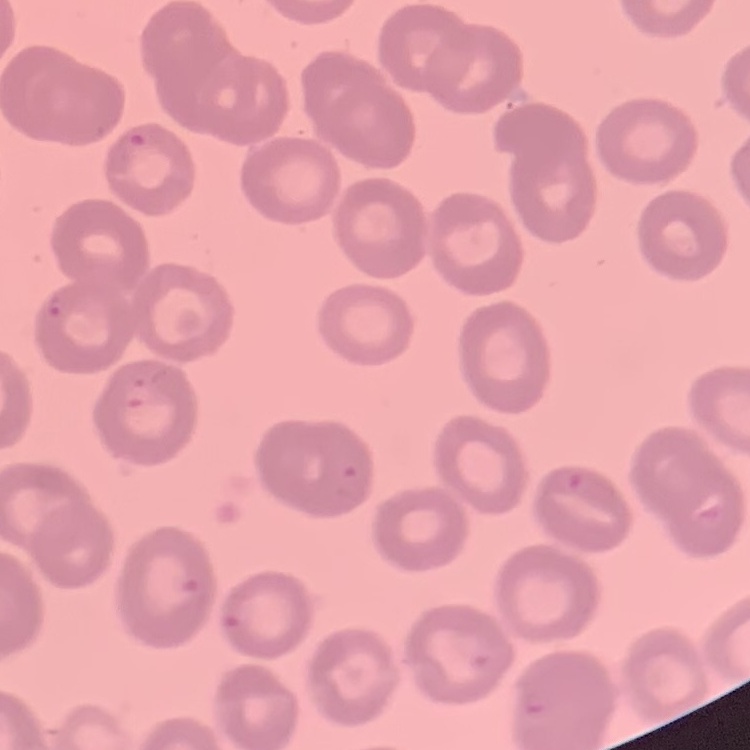
Summary:
  - Erythrocyte morphology: no rouleaux formation
  - Stain: Field's or Giemsa
  - Preparation: thin blood film
  - Image type: square crop of a larger photomicrograph